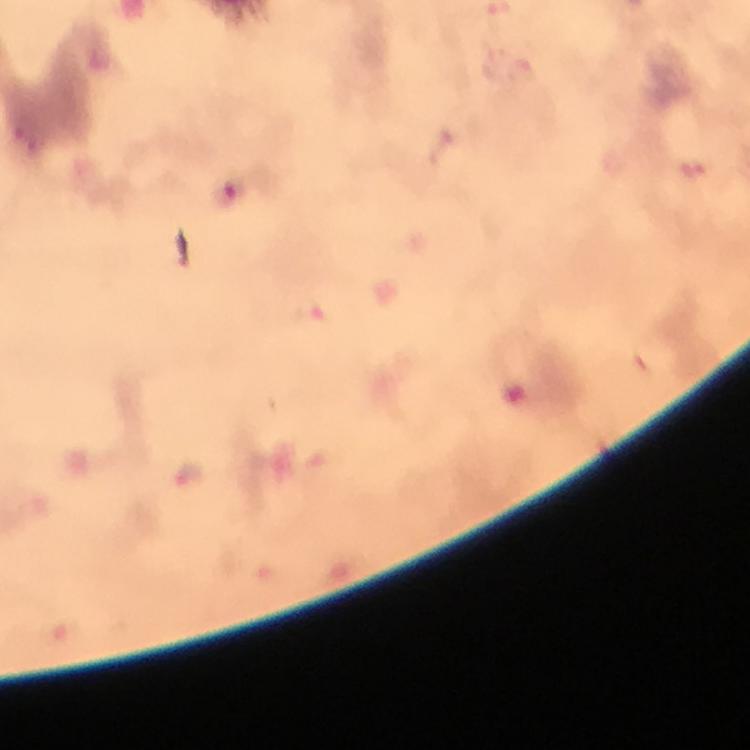

Approximate centers as (x, y) in pixels.
Summary:
  - Plasmodium parasite locations: (522, 70), (309, 311), (189, 474)
  - Image size: 750×750 pixels
  - Context: from a diagnostic examination for malaria
  - Magnification: 100x
  - Immersion oil: used
  - Cropped from: a single field of view
  - Preparation: thick smear
  - Capture: smartphone mounted on the microscope
  - Stain: Giemsa